Point out each leukocyte.
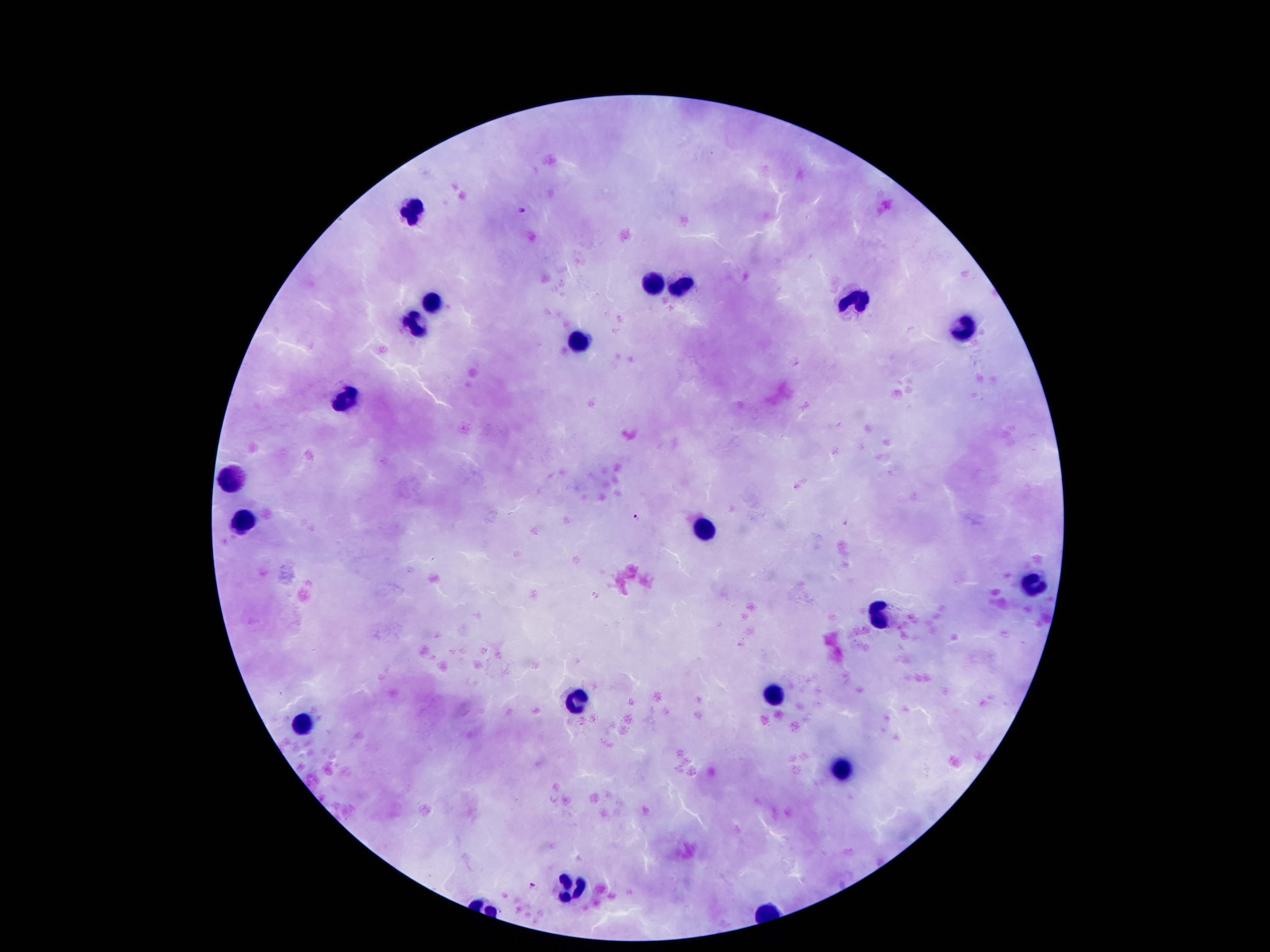

Approximate object centers, in pixels from the top-left corner.
Leukocytes: (x=413, y=210), (x=647, y=282), (x=686, y=289), (x=429, y=300), (x=859, y=302), (x=416, y=328), (x=965, y=331), (x=576, y=341), (x=349, y=395), (x=237, y=473), (x=243, y=521), (x=705, y=530), (x=1029, y=588), (x=879, y=617), (x=775, y=694), (x=576, y=704), (x=299, y=724), (x=840, y=772), (x=571, y=888).

Summary:
  - Plasmodium parasite locations: (x=522, y=210), (x=637, y=517), (x=532, y=885)
  - Magnification: 100x
  - Image size: 1270×952 pixels
  - Field of view: one from this slide
  - Stain: Giemsa
  - Capture: smartphone camera through the microscope eyepiece
  - Patient malaria status: infected with Plasmodium falciparum
  - Preparation: thick blood smear